Outline each blood parasite and name the species.
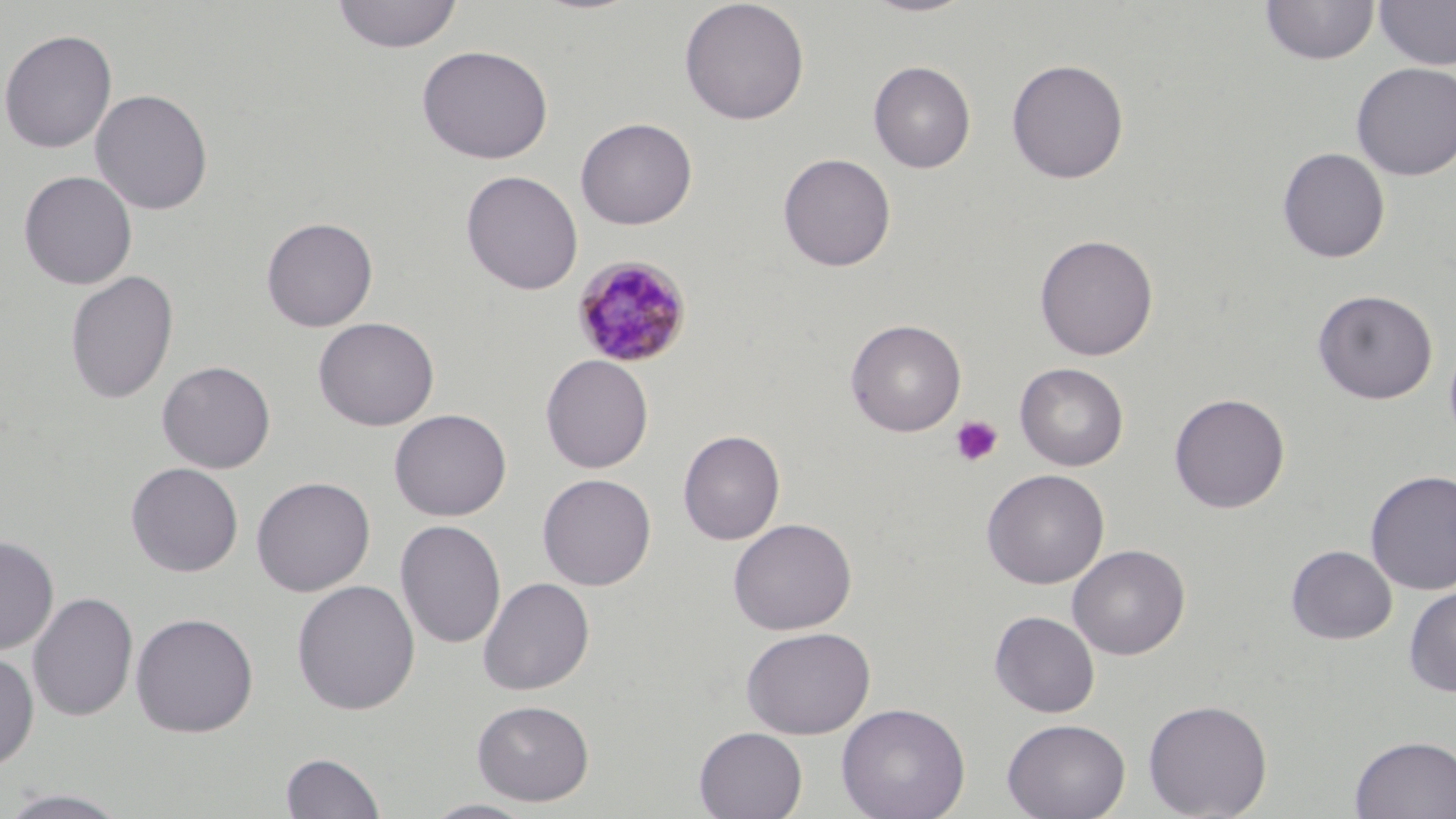

Approximate bounding boxes as (x1,y1)-(x2,y2) corner pairs in pixels.
Plasmodium malariae-infected red blood cells: (571,254)-(694,368).
No Plasmodium falciparum, Plasmodium ovale, Plasmodium vivax, Babesia divergens, or Trypanosoma brucei observed.

Platelet locations: (949,415)-(1003,468). Uninfected red blood cell locations: (331,0)-(463,53), (678,0)-(810,125), (861,0)-(979,18), (1374,0)-(1456,70), (1260,1)-(1379,66), (0,29)-(118,154), (416,45)-(553,164), (1006,58)-(1130,184), (868,60)-(976,173), (1351,63)-(1456,181), (90,88)-(213,216), (575,117)-(697,230), (1277,147)-(1390,263), (778,153)-(896,271), (18,170)-(138,290), (461,170)-(583,295), (261,216)-(378,332), (1034,234)-(1159,361), (64,270)-(179,405), (1313,289)-(1438,404), (313,316)-(440,431), (845,318)-(967,437), (540,354)-(654,473), (156,360)-(276,473), (1014,363)-(1129,471), (1170,392)-(1290,513), (389,408)-(512,521), (678,429)-(786,545), (126,462)-(244,577), (981,469)-(1109,589), (1364,469)-(1456,595), (537,473)-(657,590), (251,476)-(375,597), (728,518)-(857,635), (395,519)-(506,649), (0,535)-(59,655), (1067,544)-(1190,660), (1286,545)-(1397,645), (478,576)-(595,695), (291,579)-(420,715), (1404,584)-(1456,697), (27,591)-(139,722), (989,610)-(1100,718), (131,612)-(259,737), (740,625)-(876,739), (0,649)-(40,772), (1142,698)-(1273,818), (472,699)-(595,805), (836,702)-(970,819), (1002,718)-(1130,819), (694,726)-(808,819), (1350,735)-(1456,818), (280,751)-(386,818), (0,787)-(135,818), (421,798)-(539,818). Slide-level diagnosis: Plasmodium malariae. Single field of view. Light microscopy. Captured at 1000x magnification. Thin blood film. Image is 1456×819 pixels. May-Grünwald-Giemsa-stained preparation.